State the blood parasite species.
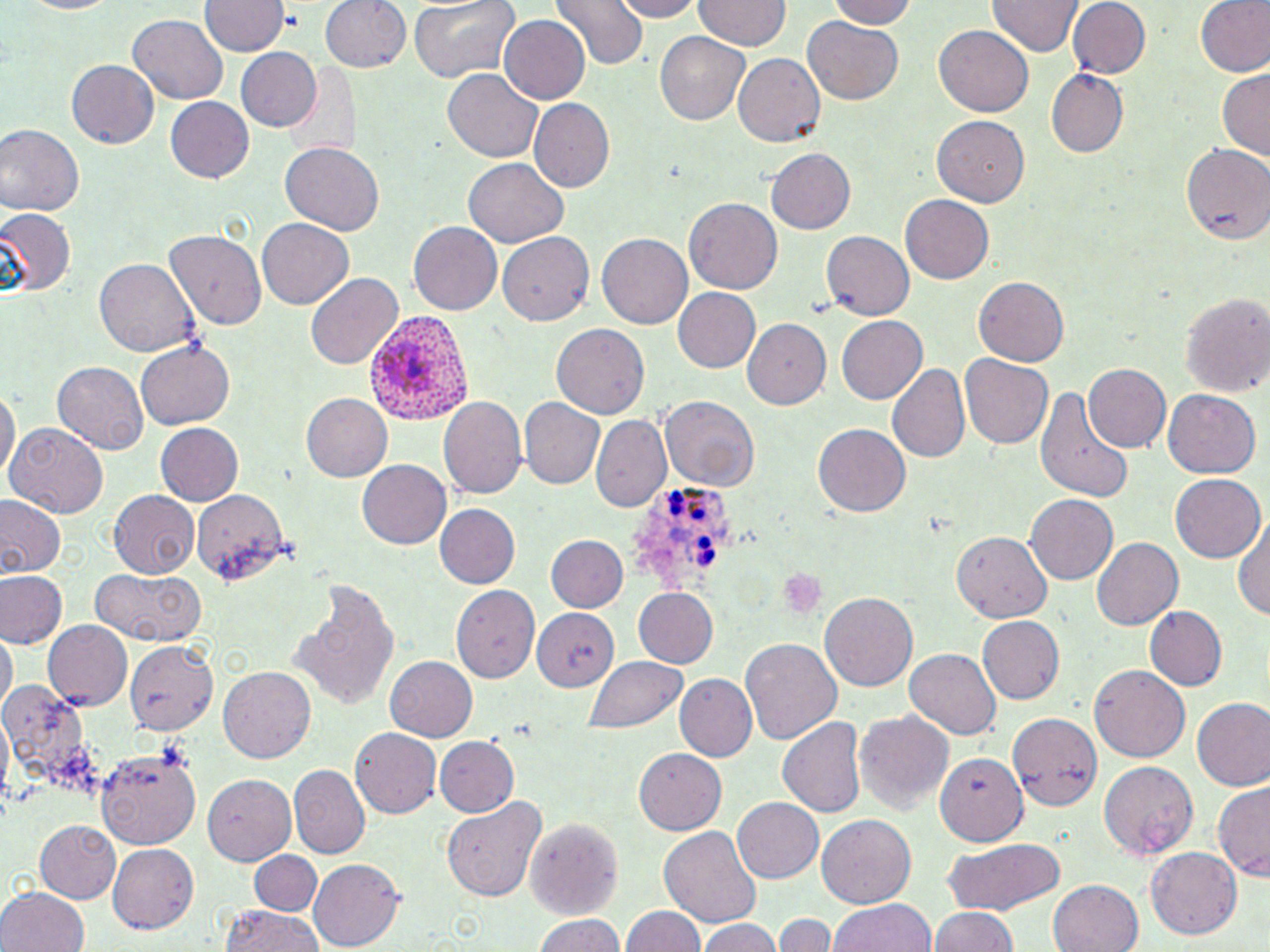
Plasmodium ovale.

Approximate bounding boxes as (x1,y1)-(x2,y2) corner pairs in pixels. Plasmodium ovale-infected red blood cell locations: (369,308)-(473,426), (635,489)-(741,587). Platelet locations: (777,567)-(826,620). Uninfected red blood cell locations: (201,0)-(287,59), (319,0)-(411,73), (406,0)-(522,83), (606,0)-(705,22), (823,0)-(918,28), (989,0)-(1083,59), (1066,0)-(1150,79), (1194,0)-(1270,79), (550,1)-(648,71), (693,1)-(792,52), (128,15)-(229,104), (499,15)-(591,105), (803,17)-(903,105), (933,24)-(1036,116), (656,33)-(750,124), (233,46)-(322,133), (734,53)-(827,147), (65,58)-(159,149), (283,62)-(358,159), (1216,67)-(1270,164), (442,69)-(544,162), (1049,72)-(1128,156), (164,97)-(255,183), (529,100)-(613,190), (931,113)-(1029,206), (0,125)-(82,218), (280,142)-(385,236), (1182,143)-(1270,246), (766,148)-(856,234), (462,160)-(567,248), (899,192)-(993,281), (684,198)-(783,293), (0,209)-(74,296), (256,218)-(354,310), (407,222)-(501,315), (820,230)-(914,319), (165,231)-(267,329), (498,231)-(592,325), (596,234)-(691,330), (96,258)-(198,357), (305,272)-(404,369), (973,277)-(1070,367), (672,288)-(762,373), (1179,290)-(1268,396), (833,315)-(928,406), (745,318)-(832,405), (552,322)-(651,418), (137,341)-(235,429), (960,355)-(1052,449), (53,361)-(148,455), (886,362)-(971,464), (1082,363)-(1170,454), (0,381)-(18,489), (1035,383)-(1135,502), (1161,389)-(1259,477), (300,392)-(393,482), (440,396)-(527,499), (519,397)-(606,488), (662,397)-(756,488), (591,413)-(671,512), (6,420)-(108,519), (155,425)-(242,504), (813,425)-(911,517), (357,460)-(451,550), (1168,474)-(1265,562), (190,489)-(289,585), (107,490)-(200,577), (1025,491)-(1118,582), (0,495)-(65,581), (435,504)-(521,589), (1233,519)-(1270,622), (953,529)-(1053,622), (548,535)-(628,612), (1089,537)-(1183,631), (90,567)-(207,647), (0,571)-(66,649), (292,580)-(401,712), (453,584)-(542,683), (631,586)-(719,669), (819,592)-(917,693), (1142,606)-(1227,692), (530,607)-(621,687), (976,615)-(1065,704), (41,619)-(132,709), (1,629)-(16,718), (740,638)-(844,748), (121,642)-(219,735), (904,648)-(1002,741), (385,655)-(478,742), (585,655)-(689,733), (1089,666)-(1189,762), (219,668)-(315,762), (677,674)-(757,762), (1,681)-(96,784), (1192,698)-(1270,791), (856,712)-(955,816), (1008,712)-(1102,809), (777,716)-(868,817), (352,729)-(440,818), (434,735)-(518,817), (96,747)-(200,847), (634,748)-(726,835), (936,754)-(1026,846), (1099,763)-(1196,860), (289,767)-(369,857), (201,773)-(297,866), (1214,781)-(1270,882), (440,795)-(547,904), (733,798)-(823,882), (817,814)-(916,906), (522,816)-(624,921), (34,818)-(121,904), (659,825)-(762,927), (941,838)-(1067,914), (106,841)-(198,933), (1146,849)-(1243,940), (250,851)-(321,915), (308,859)-(404,950), (1049,878)-(1145,952), (1,886)-(91,952), (827,897)-(936,952), (220,903)-(325,952), (621,905)-(703,952), (929,908)-(1019,952), (776,913)-(835,952), (530,914)-(631,952), (697,919)-(783,952). One field of a larger specimen. May-Grünwald-Giemsa-stained preparation. Thin blood smear. Captured at 1000x magnification. Optical microscopy. Image is 1270×952 pixels.